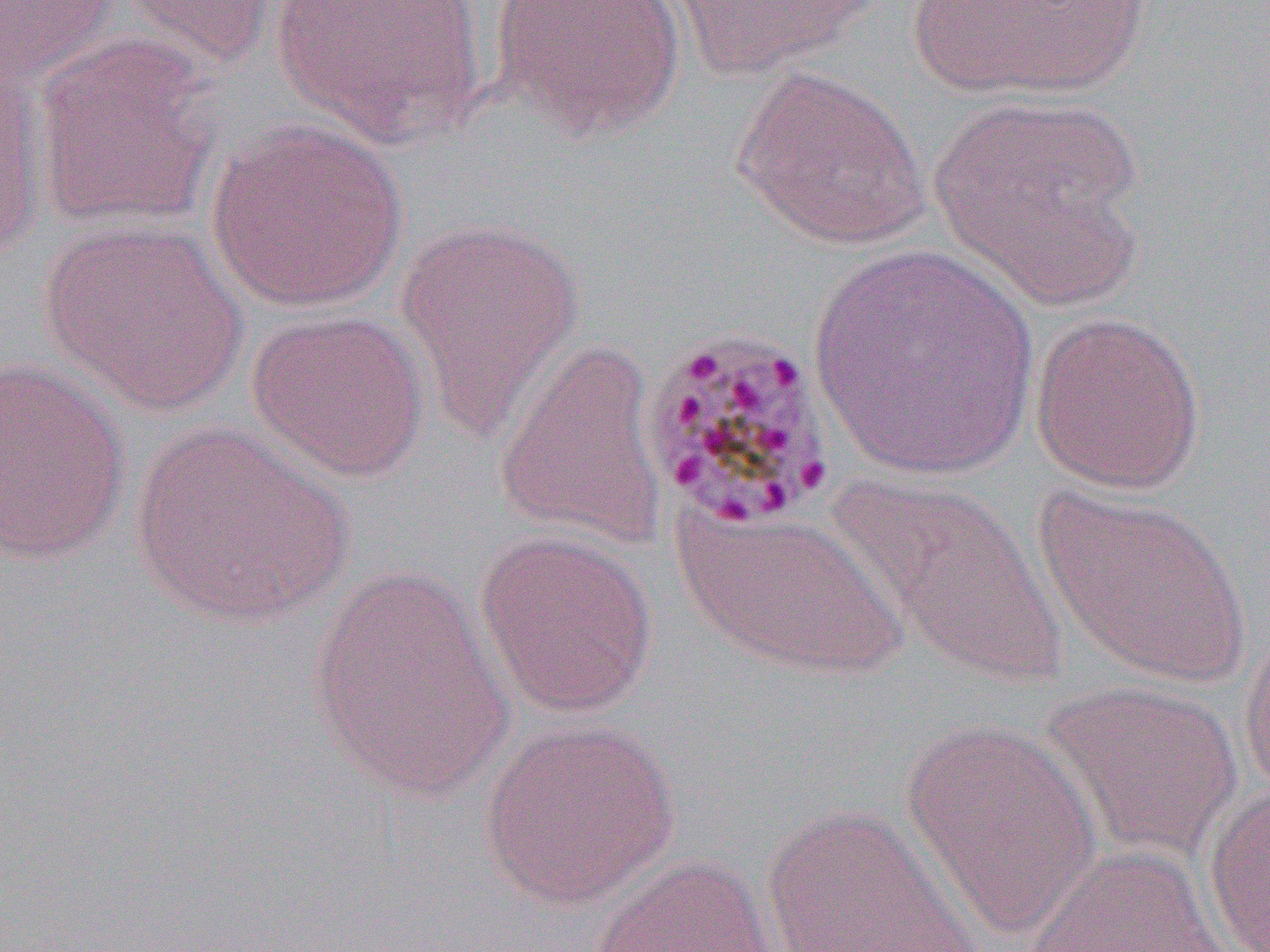
slide-level diagnosis = Plasmodium malariae
uninfected red blood cell locations = approximate bounding boxes as (x1,y1)-(x2,y2) corner pairs in pixels: (106,0)-(279,74), (269,0)-(490,148), (490,0)-(687,141), (667,0)-(881,79), (1,1)-(119,92), (910,1)-(1152,99), (31,36)-(220,229), (0,59)-(46,263), (731,64)-(931,251), (929,93)-(1147,297), (205,119)-(410,313), (394,216)-(586,439), (39,219)-(246,413), (810,242)-(1036,481), (246,308)-(430,481), (1029,311)-(1206,495), (493,337)-(670,551), (0,359)-(131,565), (130,423)-(352,626), (832,471)-(1069,690), (1034,484)-(1252,688), (673,505)-(912,681), (473,529)-(660,720), (308,564)-(516,801), (1238,616)-(1270,802), (1039,679)-(1243,864), (900,717)-(1101,937), (479,718)-(681,909), (1203,781)-(1270,952), (760,804)-(984,951), (1020,844)-(1233,952), (588,853)-(777,952)
modality = light microscopy
field of view = one of a larger specimen
magnification = 1000x
image size = 1270×952 pixels
preparation = thin blood film